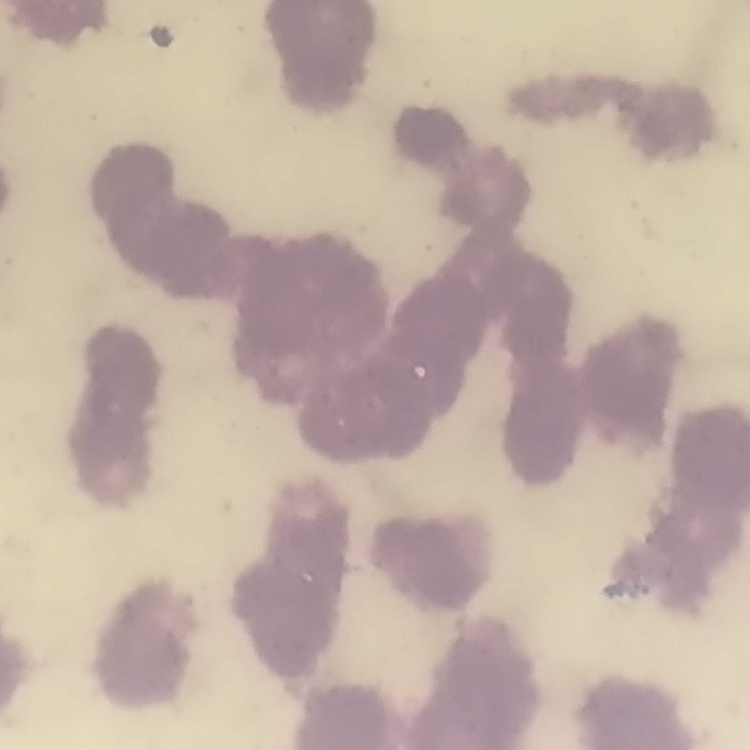
red_blood_cell_morphology: rouleaux formation
preparation: thin blood smear
stain: Field's or Giemsa
image_type: one tile cut from a larger photomicrograph